Assess this cell for malaria.
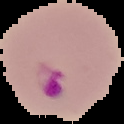

Parasitized.

Summary:
  - Preparation: thin blood smear
  - Image size: 124×124 pixels
  - Image type: segmented cell region on a black background